Locate and identify every blood parasite.
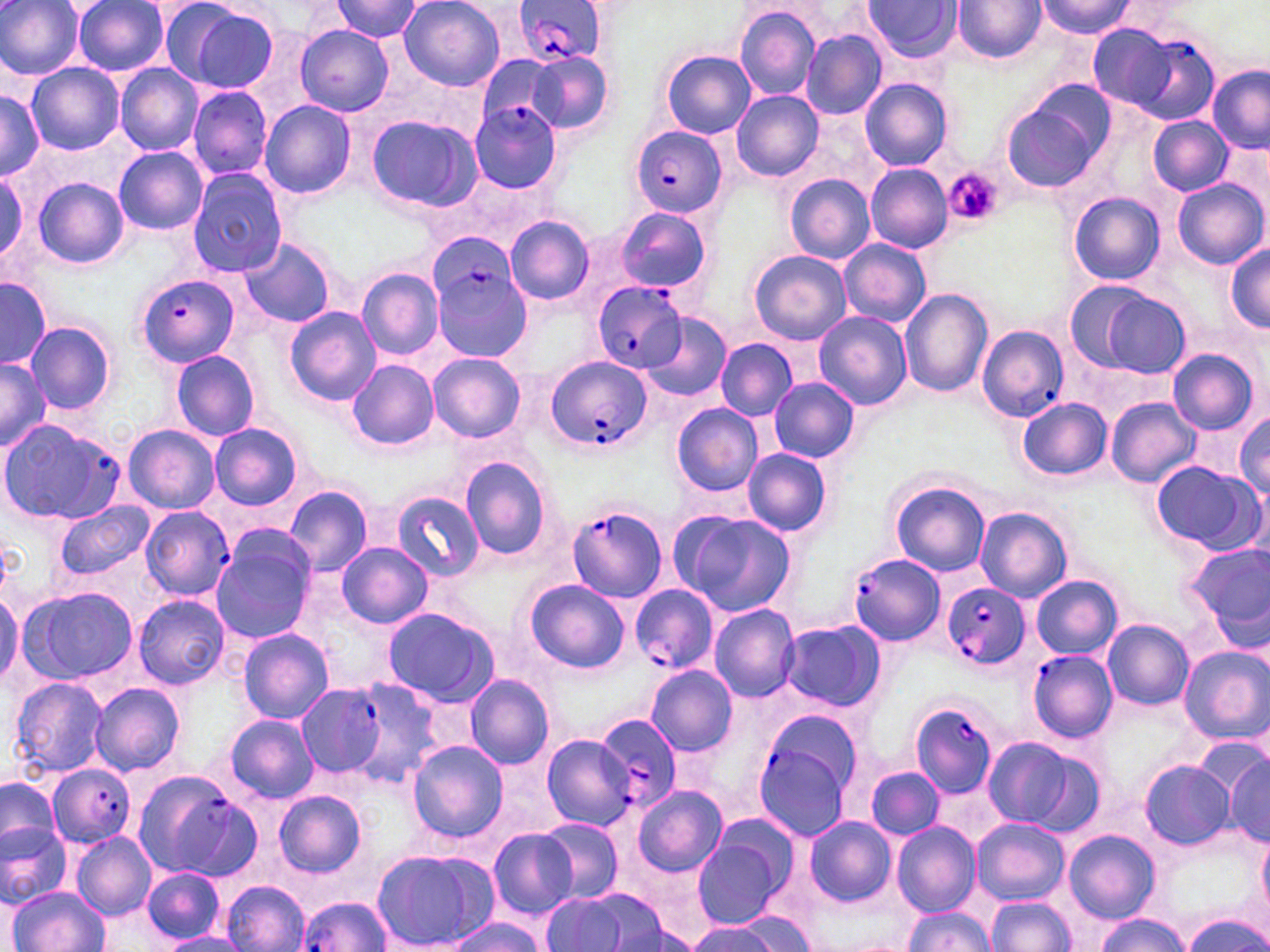
Approximate bounding boxes as (x1, y1, x2, y2) in pixels.
Plasmodium falciparum-infected red blood cells: (510, 0, 610, 67), (1133, 32, 1219, 126), (470, 100, 561, 193), (630, 126, 727, 215), (428, 234, 518, 316), (432, 257, 531, 363), (135, 274, 240, 368), (594, 282, 688, 371), (976, 324, 1068, 422), (544, 354, 651, 453), (0, 419, 124, 525), (567, 504, 668, 600), (140, 506, 235, 600), (847, 552, 946, 644), (941, 582, 1028, 673), (630, 584, 718, 675), (1027, 648, 1117, 743), (296, 685, 388, 775), (909, 700, 1000, 799), (751, 710, 863, 839), (594, 711, 685, 811), (49, 764, 134, 848), (132, 770, 242, 874), (298, 896, 390, 951).
No Plasmodium ovale, Plasmodium malariae, Plasmodium vivax, Babesia divergens, or Trypanosoma brucei observed.

Uninfected red blood cell locations: (400, 0, 506, 92), (866, 0, 961, 62), (1040, 0, 1133, 40), (0, 1, 85, 79), (331, 1, 425, 42), (953, 1, 1046, 63), (73, 2, 169, 76), (180, 4, 282, 94), (735, 6, 820, 101), (1088, 23, 1181, 111), (296, 26, 393, 115), (801, 29, 886, 120), (659, 50, 756, 140), (526, 52, 613, 134), (478, 56, 568, 133), (26, 62, 123, 154), (115, 63, 203, 154), (1207, 65, 1269, 152), (1183, 77, 1265, 189), (859, 79, 953, 169), (187, 85, 273, 181), (0, 89, 43, 180), (731, 89, 823, 181), (259, 100, 357, 199), (1001, 102, 1103, 193), (364, 114, 481, 215), (1149, 117, 1232, 195), (113, 146, 209, 234), (866, 164, 953, 253), (0, 166, 27, 264), (189, 168, 288, 276), (785, 174, 876, 263), (33, 178, 130, 268), (1172, 179, 1266, 269), (1069, 192, 1164, 285), (616, 208, 712, 294), (505, 215, 594, 305), (239, 237, 338, 328), (838, 239, 930, 327), (1224, 245, 1270, 331), (748, 250, 851, 345), (357, 269, 443, 360), (0, 278, 51, 369), (1063, 279, 1156, 372), (899, 288, 993, 398), (1100, 292, 1190, 379), (284, 306, 381, 406), (814, 311, 911, 409), (643, 312, 731, 403), (26, 322, 115, 415), (715, 339, 797, 421), (170, 348, 259, 442), (1168, 349, 1259, 435), (429, 352, 526, 444), (0, 358, 52, 450), (347, 359, 440, 450), (770, 378, 859, 463), (1018, 397, 1113, 480), (1105, 397, 1201, 487), (672, 403, 763, 497), (1231, 413, 1270, 498), (209, 421, 304, 512), (122, 425, 219, 513), (742, 448, 833, 538), (459, 454, 553, 561), (1150, 461, 1265, 556), (889, 479, 990, 577), (285, 484, 373, 577), (392, 491, 484, 581), (54, 502, 153, 580), (976, 507, 1071, 603), (672, 512, 797, 617), (210, 529, 318, 645), (336, 541, 432, 628), (1185, 541, 1269, 640), (1030, 575, 1122, 660), (524, 579, 630, 675), (19, 587, 137, 685), (0, 590, 22, 690), (134, 595, 229, 690), (709, 603, 800, 702), (383, 607, 500, 708), (1103, 619, 1194, 710), (780, 621, 885, 713), (237, 628, 335, 723), (1179, 647, 1270, 743), (646, 663, 738, 757), (464, 675, 554, 769), (8, 676, 109, 779), (323, 676, 443, 786), (89, 683, 185, 775), (225, 715, 319, 802), (540, 733, 638, 832), (982, 737, 1085, 829), (407, 741, 507, 844), (1219, 751, 1270, 846), (1138, 759, 1235, 849), (867, 765, 944, 839), (0, 778, 61, 851), (632, 786, 727, 877), (275, 790, 367, 877), (802, 818, 896, 907), (971, 818, 1070, 905), (537, 819, 623, 901), (0, 821, 71, 906), (892, 822, 980, 915), (489, 829, 579, 918), (688, 829, 793, 930), (1065, 829, 1160, 924), (72, 832, 157, 919), (1257, 833, 1270, 917), (370, 848, 497, 951), (141, 867, 226, 943), (221, 881, 309, 952), (9, 887, 106, 952), (562, 887, 675, 951), (542, 893, 629, 949), (986, 897, 1076, 951), (902, 906, 991, 951), (727, 907, 824, 952), (1181, 913, 1270, 952), (1096, 914, 1191, 952), (449, 918, 546, 952), (686, 921, 787, 951), (159, 933, 246, 952). Platelet locations: (943, 169, 1001, 226). Slide-level diagnosis: Plasmodium falciparum. 1000x magnification. Single field of view. Image is 1270×952 pixels. May-Grünwald-Giemsa-stained preparation. Thin blood smear. Light microscopy.